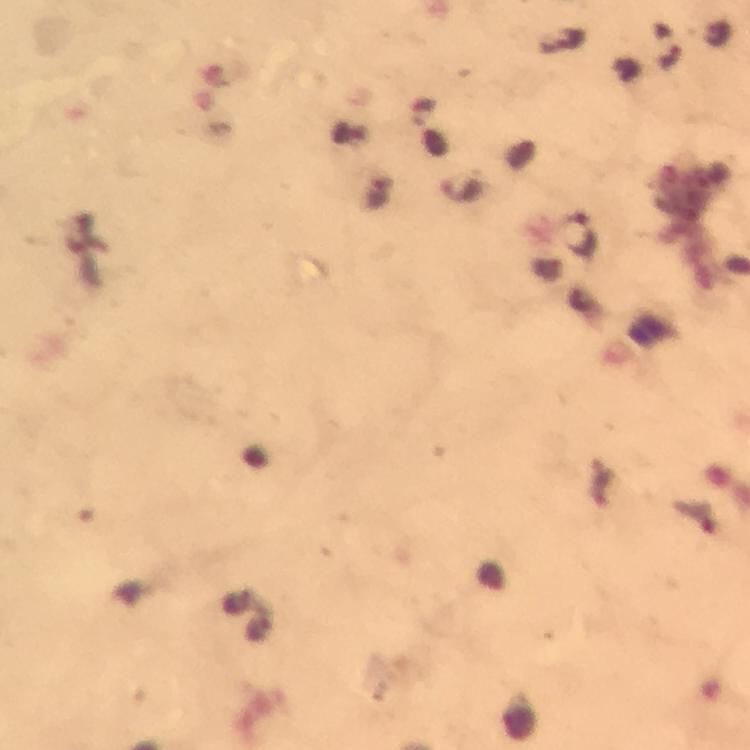 Approximate centers as [x, y] in pixels. Malaria parasite locations: [463, 189], [580, 237]. Cropped region of a single field of view. 100x magnification. Thick blood film. From a diagnostic examination for malaria. Immersion oil applied. Giemsa-stained preparation. Image is 750×750 pixels. Smartphone photograph taken through a microscope.